Report the malaria status of this cell.
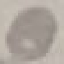

Uninfected.

Giemsa-stained preparation. Automatically extracted cell patch, resized to 64 × 64 pixels. Thin blood smear. Acquired by smartphone through the microscope eyepiece.